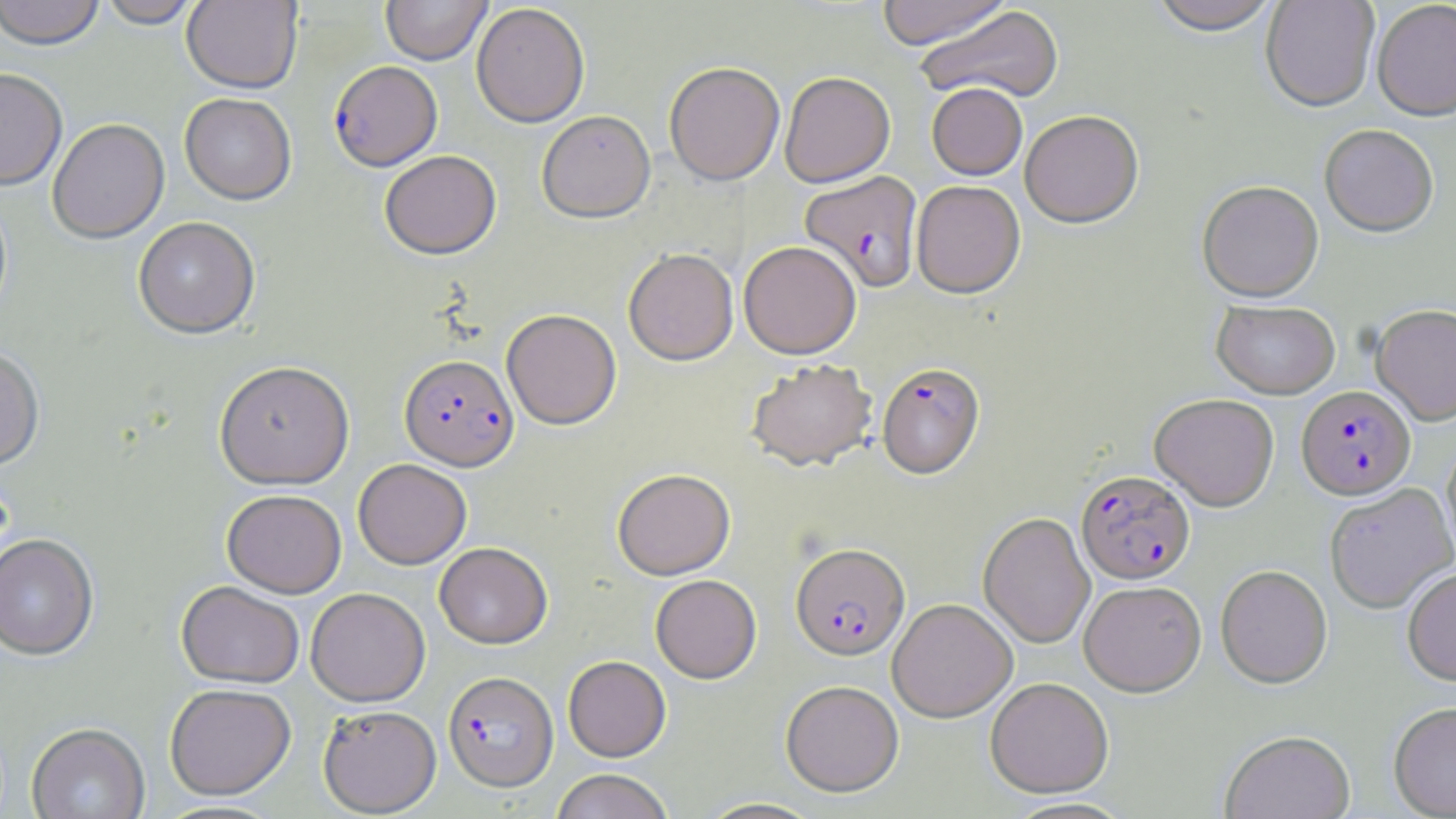
Summary:
  - Coordinate format: approximate bounding boxes as named x1/y1/x2/y2 corners in pixels
  - Uninfected red blood cell locations: (x1=0, y1=0, x2=105, y2=52), (x1=99, y1=0, x2=201, y2=30), (x1=182, y1=0, x2=303, y2=95), (x1=380, y1=0, x2=492, y2=67), (x1=875, y1=0, x2=1013, y2=50), (x1=1149, y1=0, x2=1281, y2=38), (x1=1260, y1=0, x2=1380, y2=115), (x1=1372, y1=2, x2=1456, y2=124), (x1=472, y1=4, x2=590, y2=129), (x1=915, y1=6, x2=1066, y2=105), (x1=664, y1=63, x2=785, y2=187), (x1=0, y1=70, x2=68, y2=193), (x1=779, y1=72, x2=895, y2=188), (x1=927, y1=84, x2=1027, y2=181), (x1=179, y1=94, x2=296, y2=207), (x1=537, y1=113, x2=656, y2=225), (x1=1020, y1=113, x2=1144, y2=230), (x1=48, y1=121, x2=170, y2=246), (x1=1319, y1=127, x2=1439, y2=240), (x1=380, y1=152, x2=502, y2=261), (x1=912, y1=181, x2=1026, y2=300), (x1=1197, y1=183, x2=1324, y2=305), (x1=133, y1=218, x2=260, y2=341), (x1=739, y1=241, x2=862, y2=359), (x1=623, y1=248, x2=738, y2=366), (x1=1212, y1=302, x2=1340, y2=399), (x1=1371, y1=306, x2=1456, y2=426), (x1=502, y1=310, x2=621, y2=430), (x1=0, y1=350, x2=45, y2=471), (x1=746, y1=359, x2=877, y2=473), (x1=214, y1=363, x2=355, y2=491), (x1=1149, y1=394, x2=1279, y2=511), (x1=1441, y1=441, x2=1456, y2=565), (x1=353, y1=459, x2=471, y2=570), (x1=612, y1=469, x2=735, y2=581), (x1=1325, y1=484, x2=1455, y2=615), (x1=221, y1=490, x2=347, y2=599), (x1=977, y1=513, x2=1095, y2=649), (x1=0, y1=536, x2=99, y2=663), (x1=434, y1=542, x2=552, y2=649), (x1=1216, y1=566, x2=1332, y2=688), (x1=1402, y1=568, x2=1456, y2=687), (x1=650, y1=575, x2=761, y2=684), (x1=176, y1=582, x2=304, y2=689), (x1=1079, y1=582, x2=1206, y2=697), (x1=306, y1=588, x2=430, y2=707), (x1=888, y1=599, x2=1018, y2=722), (x1=563, y1=656, x2=671, y2=762), (x1=985, y1=678, x2=1113, y2=799), (x1=780, y1=680, x2=904, y2=797), (x1=165, y1=684, x2=296, y2=800), (x1=1388, y1=702, x2=1456, y2=818), (x1=318, y1=705, x2=441, y2=817), (x1=27, y1=724, x2=150, y2=819), (x1=1219, y1=730, x2=1356, y2=819), (x1=550, y1=769, x2=675, y2=819), (x1=694, y1=798, x2=826, y2=818)
  - Plasmodium falciparum-infected red blood cell locations: (x1=329, y1=63, x2=442, y2=173), (x1=800, y1=171, x2=924, y2=293), (x1=400, y1=355, x2=519, y2=471), (x1=877, y1=363, x2=985, y2=480), (x1=1297, y1=386, x2=1415, y2=500), (x1=1077, y1=471, x2=1195, y2=585), (x1=790, y1=544, x2=910, y2=662), (x1=443, y1=671, x2=558, y2=791)
  - Slide-level diagnosis: Plasmodium falciparum
  - Stain: May-Grünwald-Giemsa
  - Preparation: thin blood film
  - Field of view: single
  - Magnification: 1000x
  - Modality: optical microscopy
  - Image size: 1456×819 pixels